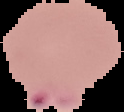
image size = 124×112 pixels
image type = cell region segmented out of the field of view; surrounding area masked to black
preparation = thin blood film
malaria status = parasitized